Name the parasite shown.
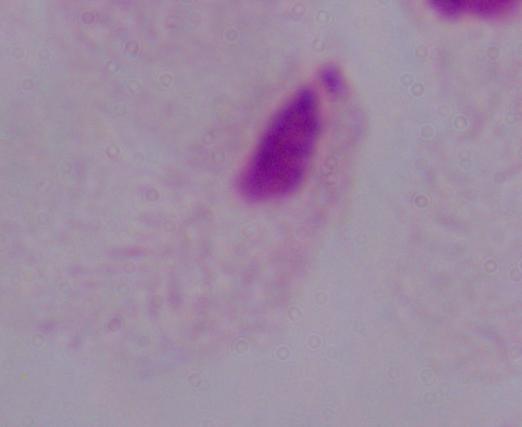
This is a trichomonad.

Summary:
  - Modality: micrograph
  - Magnification: 1000x